Name the cell type shown.
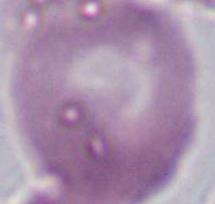

This is an erythrocyte.

Summary:
  - Magnification: 1000x
  - Modality: photomicrograph